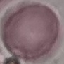
{
  "result": "negative for malaria parasites",
  "stain": "Giemsa",
  "image_type": "cell patch, automatically extracted from a larger field of view and resized to 64 × 64 pixels",
  "preparation": "thin blood film",
  "capture": "smartphone camera at the microscope eyepiece"
}